Assess the morphology of the red blood cells.
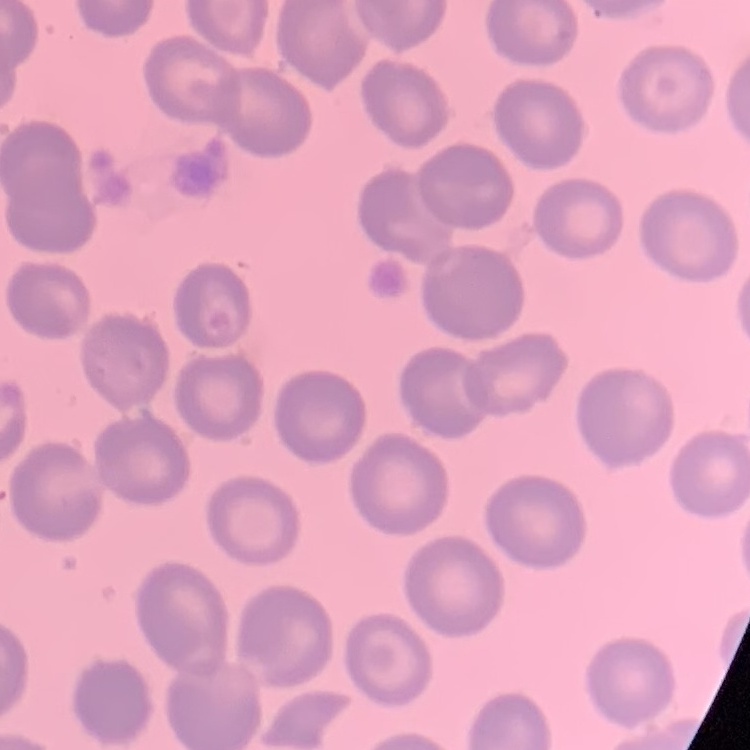
No rouleaux formation.

Summary:
  - Image type: square crop of a larger photomicrograph
  - Preparation: thin blood film
  - Stain: Field's or Giemsa